Assess the morphology of the erythrocytes.
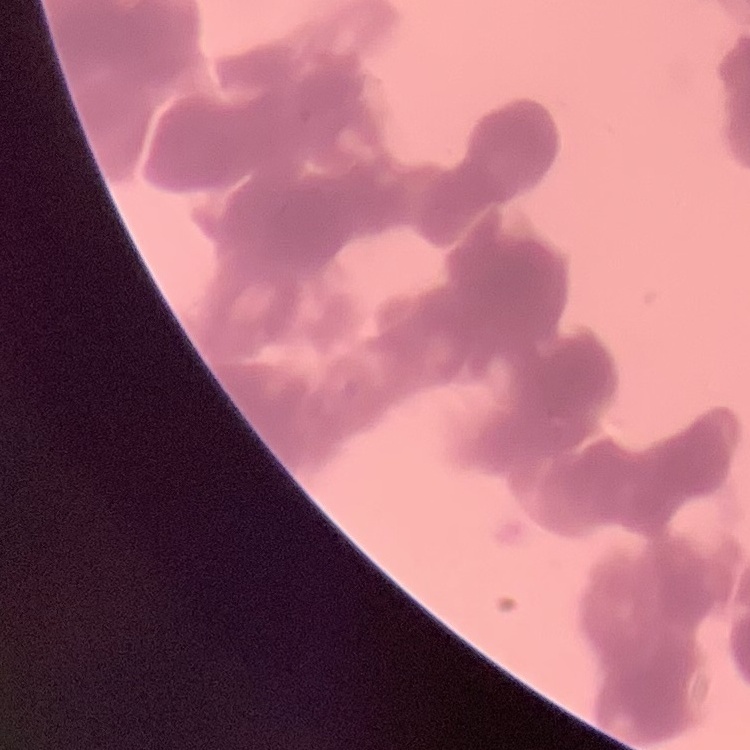
Rouleaux formation.

Field's or Giemsa stain. Thin blood film. One tile cut from a larger photomicrograph.